Name the cell type shown.
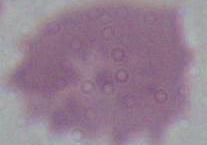

This is an erythrocyte.

1000x magnification. Photomicrograph.